Outline each blood parasite and name the species.
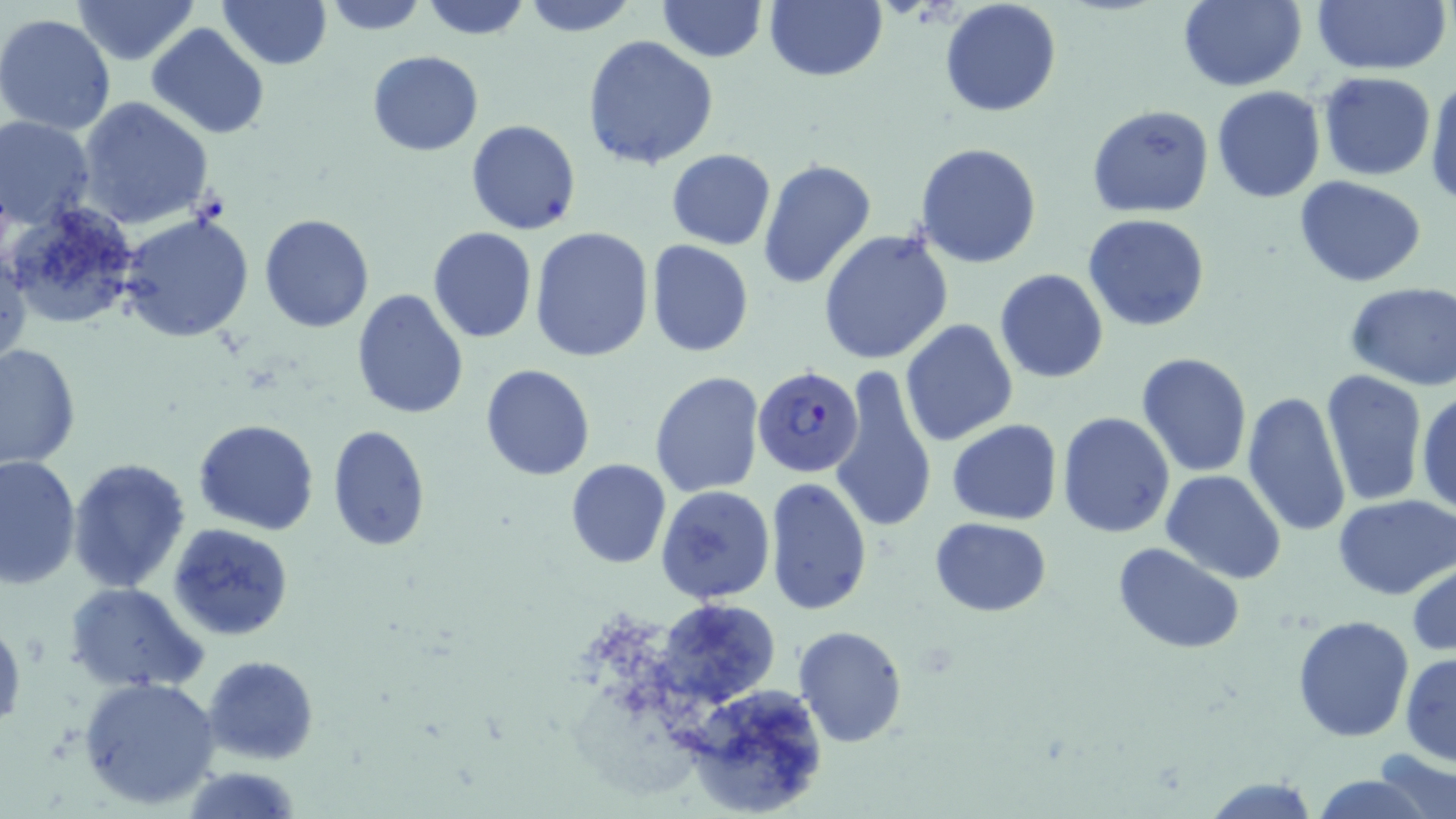

Approximate bounding boxes as [x1, y1, x2, y2] in pixels.
Plasmodium falciparum-infected red blood cells: [753, 365, 863, 477].
No Plasmodium ovale, Plasmodium malariae, Plasmodium vivax, Babesia divergens, or Trypanosoma brucei observed.

Uninfected red blood cell locations: [217, 0, 330, 70], [321, 0, 429, 35], [419, 0, 533, 40], [657, 0, 766, 61], [765, 0, 886, 82], [939, 0, 1063, 118], [1177, 0, 1306, 91], [1309, 0, 1453, 74], [72, 1, 199, 66], [522, 1, 639, 36], [0, 13, 119, 135], [146, 23, 270, 139], [582, 36, 720, 172], [368, 50, 483, 156], [1318, 70, 1436, 180], [1425, 77, 1456, 205], [1212, 85, 1325, 203], [77, 97, 217, 231], [1087, 104, 1214, 218], [0, 116, 96, 232], [466, 119, 582, 235], [913, 142, 1042, 268], [666, 148, 776, 250], [757, 160, 877, 288], [1296, 176, 1426, 288], [3, 200, 146, 327], [120, 211, 255, 343], [259, 213, 374, 332], [1084, 213, 1212, 332], [528, 225, 655, 362], [427, 228, 538, 344], [819, 229, 954, 365], [646, 240, 753, 357], [1, 246, 29, 367], [995, 268, 1108, 384], [1344, 284, 1456, 389], [352, 289, 469, 418], [900, 318, 1018, 446], [0, 342, 80, 470], [1136, 353, 1253, 478], [480, 364, 596, 481], [830, 365, 937, 535], [1320, 369, 1426, 506], [649, 371, 764, 498], [1416, 388, 1456, 517], [1242, 390, 1353, 539], [1057, 411, 1176, 539], [193, 419, 321, 535], [946, 419, 1063, 525], [328, 424, 431, 550], [0, 453, 81, 590], [68, 458, 193, 594], [566, 459, 671, 568], [1162, 471, 1287, 584], [764, 478, 873, 617], [655, 483, 777, 604], [1334, 494, 1456, 600], [931, 517, 1052, 616], [168, 523, 294, 642], [1114, 543, 1244, 653], [1408, 562, 1456, 656], [64, 581, 209, 693], [656, 596, 779, 707], [1293, 615, 1413, 740], [0, 618, 26, 733], [793, 626, 909, 747], [1400, 653, 1456, 765], [203, 654, 319, 764], [78, 674, 221, 811], [680, 684, 825, 818], [1373, 749, 1456, 817], [178, 766, 303, 819], [1308, 774, 1435, 818], [1200, 776, 1321, 818]. Slide-level diagnosis: Plasmodium falciparum. Image is 1456×819 pixels. Thin blood smear. Light microscopy. 1000x magnification. Single field of view. May-Grünwald-Giemsa-stained preparation.